Report the malaria status of this cell.
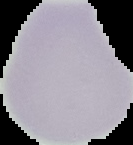
It is uninfected.

Summary:
  - Image size: 133×145 pixels
  - Preparation: thin blood smear
  - Image type: segmented cell region with the area outside set to black